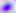

magnification = 400x
modality = photomicrograph
identification = Toxoplasma gondii